Report the malaria status of this cell.
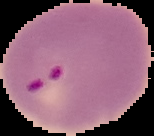

It is parasitized.

image type = segmented cell region with the area outside set to black
preparation = thin blood smear
image size = 154×136 pixels